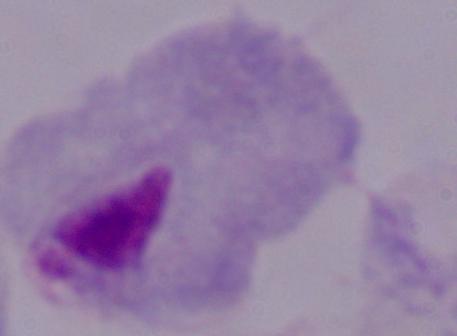
Summary:
  - Magnification: 1000x
  - Identification: trichomonad
  - Modality: photomicrograph